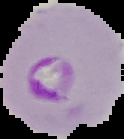

Summary:
  - Result: malaria parasites identified
  - Image size: 124×139 pixels
  - Image type: segmented cell region with the area outside set to black
  - Preparation: thin blood film